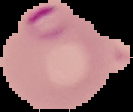
result = Plasmodium parasites detected
image type = cell region segmented out of the field of view; surrounding area masked to black
image size = 133×112 pixels
preparation = thin blood smear